Classify this cell by malaria status.
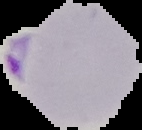
It is parasitized.

Cell region segmented out of the field of view; the surrounding area is masked to black. Image is 142×130 pixels. From a thin blood film.